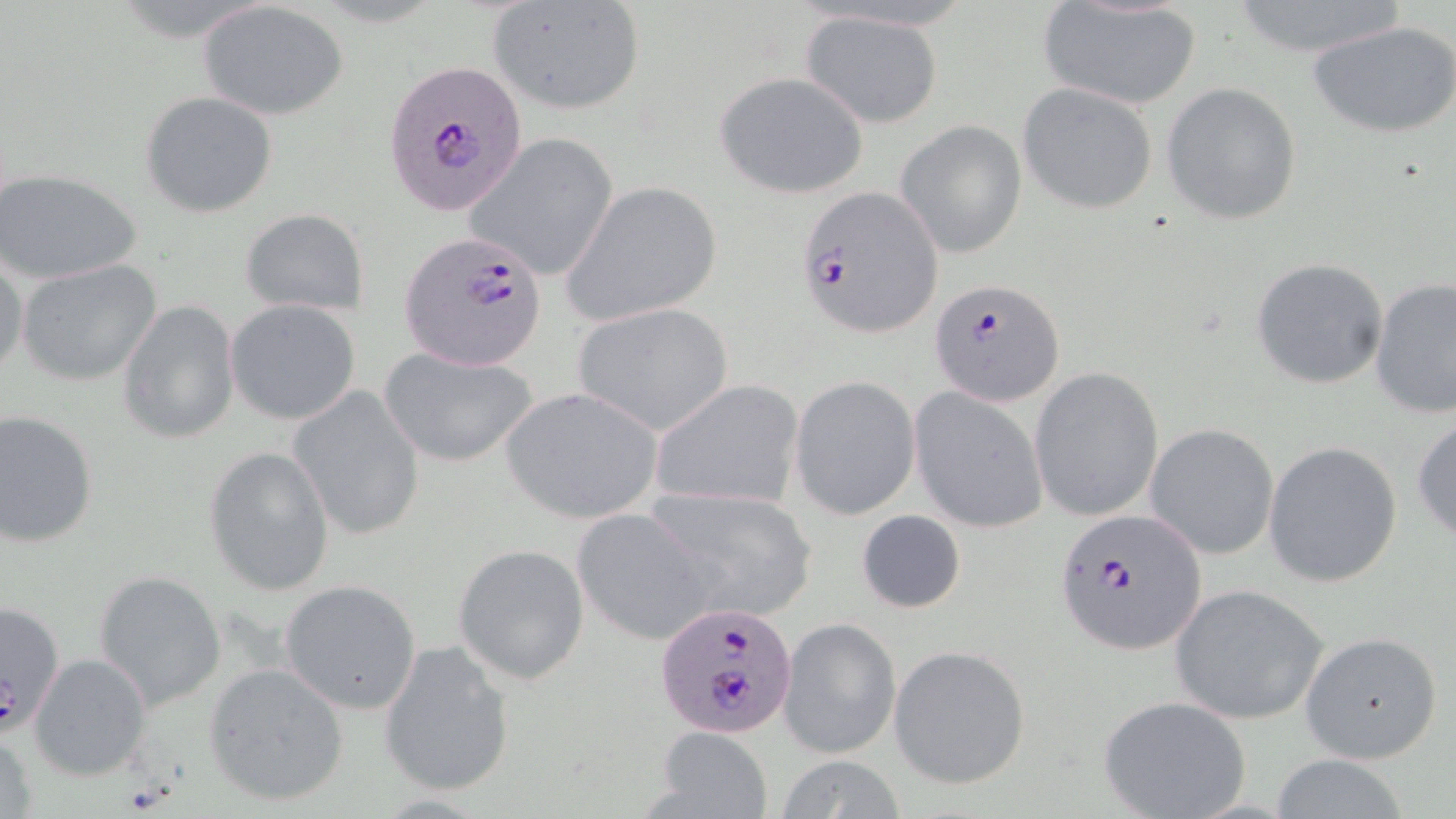 Approximate bounding boxes as (x1,y1)-(x2,y2) corner pairs in pixels. Uninfected red blood cell locations: (486,0)-(647,113), (1224,0)-(1411,60), (197,2)-(348,121), (1038,2)-(1201,110), (798,10)-(945,128), (1309,19)-(1456,139), (715,72)-(869,199), (1160,81)-(1302,225), (1017,82)-(1161,214), (140,90)-(279,217), (896,119)-(1027,260), (466,135)-(619,282), (1,169)-(143,283), (563,181)-(724,326), (239,209)-(369,315), (0,252)-(27,380), (1251,258)-(1390,389), (18,260)-(161,387), (1370,278)-(1456,417), (118,299)-(241,445), (226,299)-(363,426), (573,302)-(734,436), (377,346)-(539,467), (1030,366)-(1164,523), (791,375)-(920,519), (650,379)-(806,511), (289,383)-(426,542), (500,386)-(664,525), (909,386)-(1050,533), (0,409)-(99,548), (1411,413)-(1456,546), (1145,423)-(1279,560), (1264,440)-(1403,588), (205,445)-(335,597), (642,483)-(818,622), (855,508)-(966,615), (570,510)-(716,644), (453,543)-(590,684), (92,569)-(225,710), (280,579)-(422,714), (1170,583)-(1329,724), (1,596)-(66,739), (780,617)-(900,759), (1299,632)-(1442,763), (379,639)-(515,797), (889,645)-(1030,788), (30,654)-(150,780), (205,664)-(349,805), (1099,695)-(1250,818), (1,725)-(41,819), (651,726)-(772,818), (777,756)-(908,818), (1262,756)-(1418,818). Plasmodium falciparum-infected red blood cell locations: (393,69)-(528,212), (796,187)-(942,335), (399,230)-(554,369), (930,278)-(1066,406), (1053,506)-(1208,658), (655,601)-(800,738). Slide-level diagnosis: Plasmodium falciparum. Light microscopy. One field of a larger specimen. Thin blood smear. Image is 1456×819 pixels. May-Grünwald-Giemsa stain. 1000x magnification.